Identify the blood parasite species.
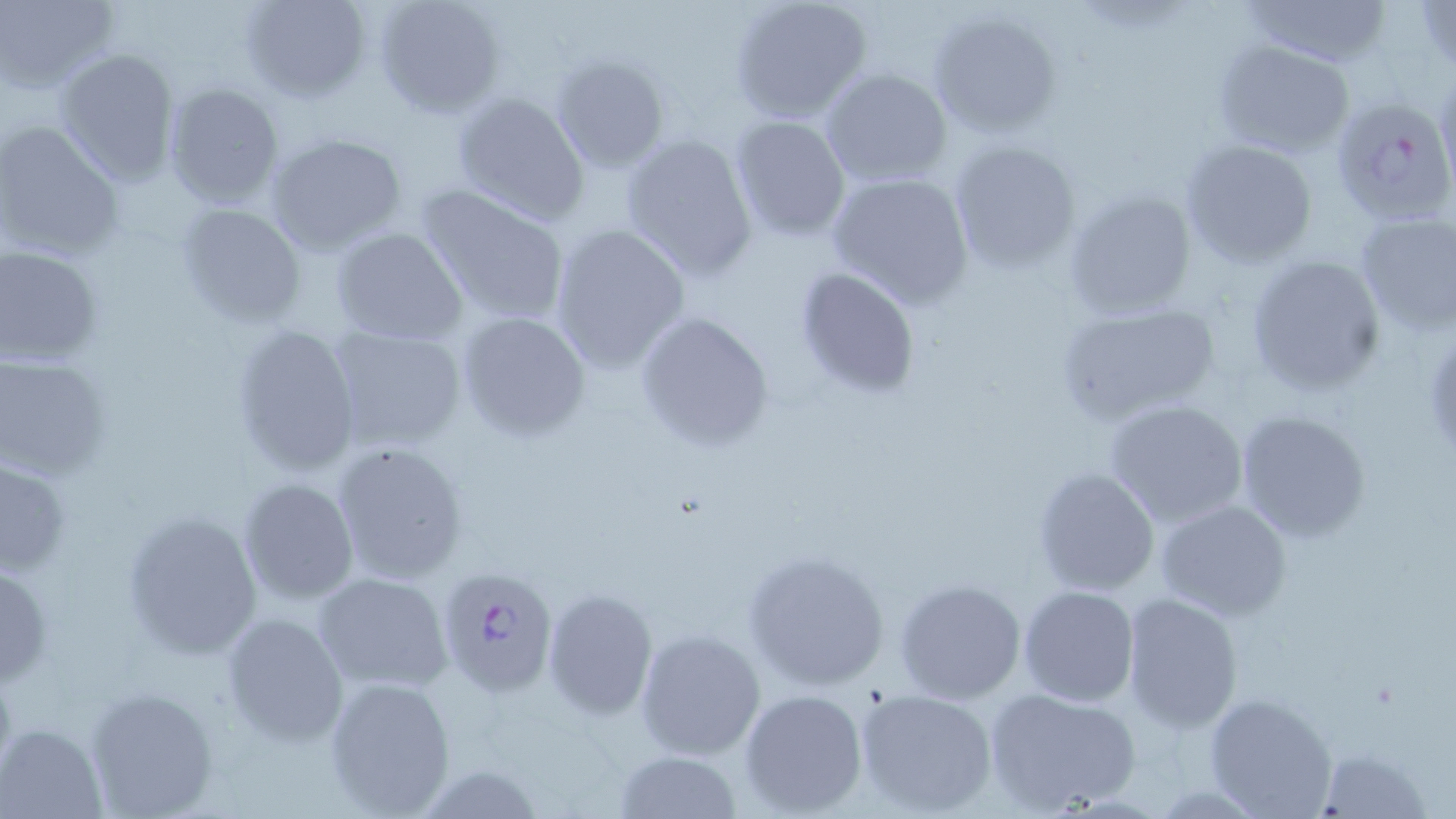

Plasmodium falciparum.

modality = light microscopy
Plasmodium falciparum-infected red blood cell locations = approximate bounding boxes as (x1, y1, x2, y2) in pixels: (1330, 95, 1456, 225), (437, 566, 558, 696)
field of view = single
stain = May-Grünwald-Giemsa
image size = 1456×819 pixels
magnification = 1000x
uninfected red blood cell locations = approximate bounding boxes as (x1, y1, x2, y2) in pixels: (239, 0, 372, 103), (371, 0, 507, 121), (728, 0, 872, 123), (1236, 0, 1394, 68), (1415, 0, 1456, 77), (1, 1, 118, 92), (927, 8, 1064, 139), (1211, 39, 1357, 160), (53, 48, 181, 186), (550, 54, 669, 172), (820, 66, 953, 187), (1434, 71, 1456, 197), (161, 82, 286, 209), (450, 90, 591, 224), (729, 116, 852, 240), (0, 121, 124, 261), (618, 131, 760, 280), (264, 133, 409, 255), (947, 138, 1081, 274), (1179, 138, 1320, 268), (826, 169, 974, 307), (416, 183, 573, 327), (1063, 187, 1199, 319), (175, 201, 307, 328), (1353, 212, 1456, 336), (547, 223, 691, 375), (330, 228, 470, 346), (0, 244, 104, 367), (1245, 254, 1387, 395), (794, 265, 923, 400), (1053, 301, 1221, 429), (455, 308, 592, 442), (633, 309, 776, 454), (228, 322, 361, 477), (326, 323, 467, 452), (0, 352, 113, 479), (1104, 397, 1249, 529), (1233, 409, 1371, 544), (331, 440, 471, 585), (0, 455, 73, 574), (1031, 466, 1161, 596), (238, 479, 359, 604), (1154, 498, 1292, 620), (119, 510, 262, 659), (742, 547, 890, 691), (0, 559, 52, 689), (312, 571, 452, 693), (895, 577, 1026, 704), (1018, 585, 1141, 708), (542, 588, 658, 720), (1121, 595, 1243, 732), (221, 611, 349, 747), (634, 629, 766, 759), (323, 675, 458, 816), (83, 684, 221, 818), (983, 684, 1142, 816), (856, 687, 998, 816), (738, 688, 870, 817), (1203, 693, 1338, 819), (2, 723, 106, 818), (1316, 747, 1432, 818), (613, 750, 743, 818), (409, 763, 552, 818)
preparation = thin blood film